Give the position of every leukocyte visible.
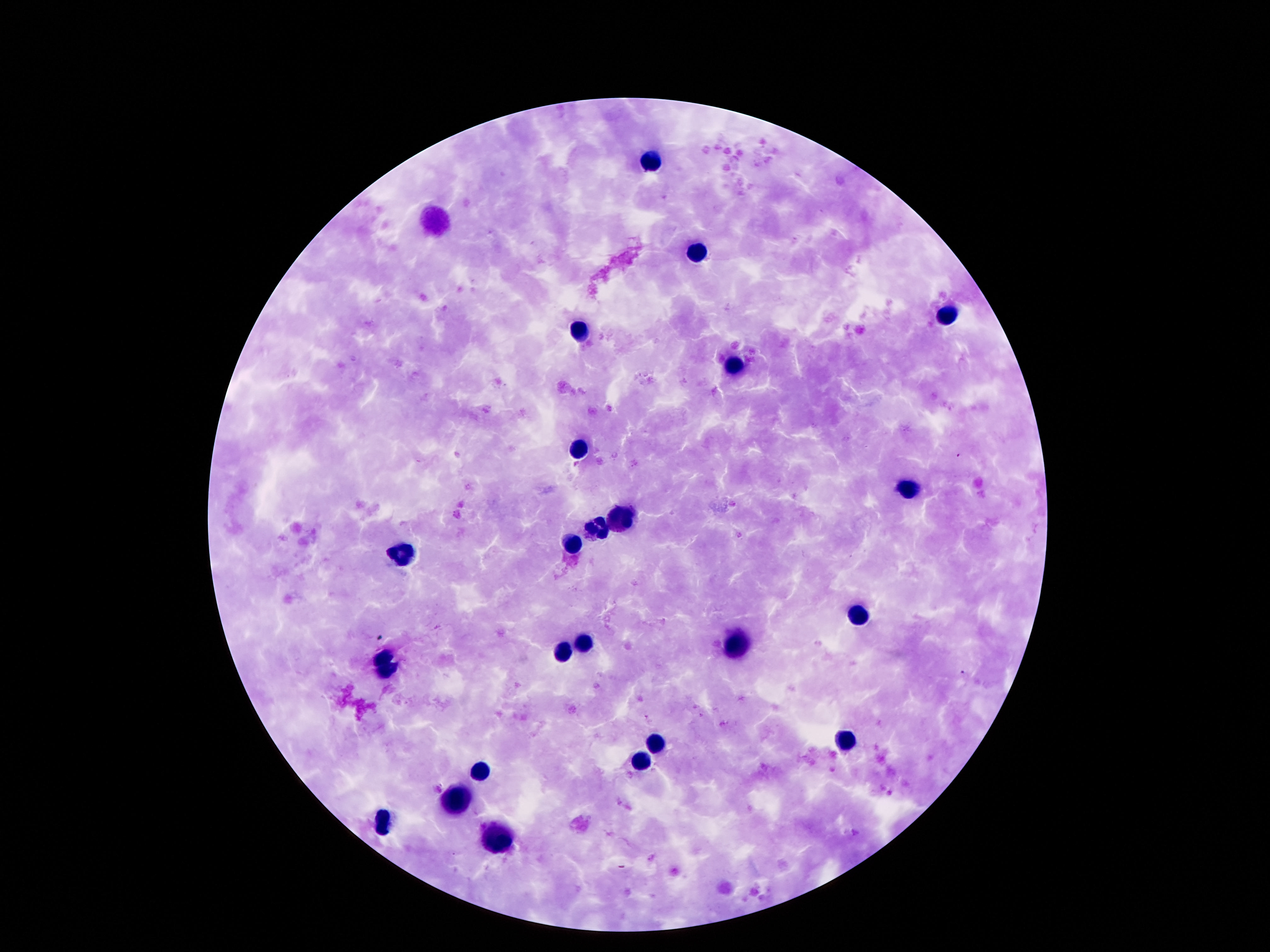
Approximate centers as [x, y] in pixels.
Leukocytes: [650, 161], [697, 252], [945, 318], [579, 332], [738, 369], [579, 451], [908, 489], [615, 517], [596, 528], [572, 545], [400, 556], [861, 617], [738, 643], [583, 644], [565, 651], [385, 664], [845, 740], [656, 744], [639, 765], [475, 774], [454, 796], [383, 822], [494, 841].

Image is 1270×952 pixels. Thick peripheral-blood smear. Smartphone photograph taken through the microscope eyepiece. Giemsa-stained preparation. Single field of view. Patient malaria status: negative. 100x magnification.